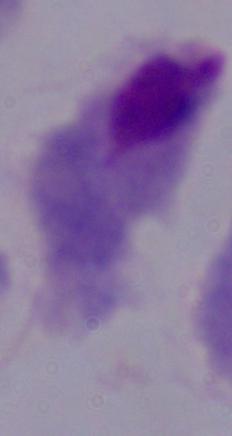

Summary:
  - Magnification: 1000x
  - Identification: trichomonad
  - Modality: photomicrograph